Assess for malaria.
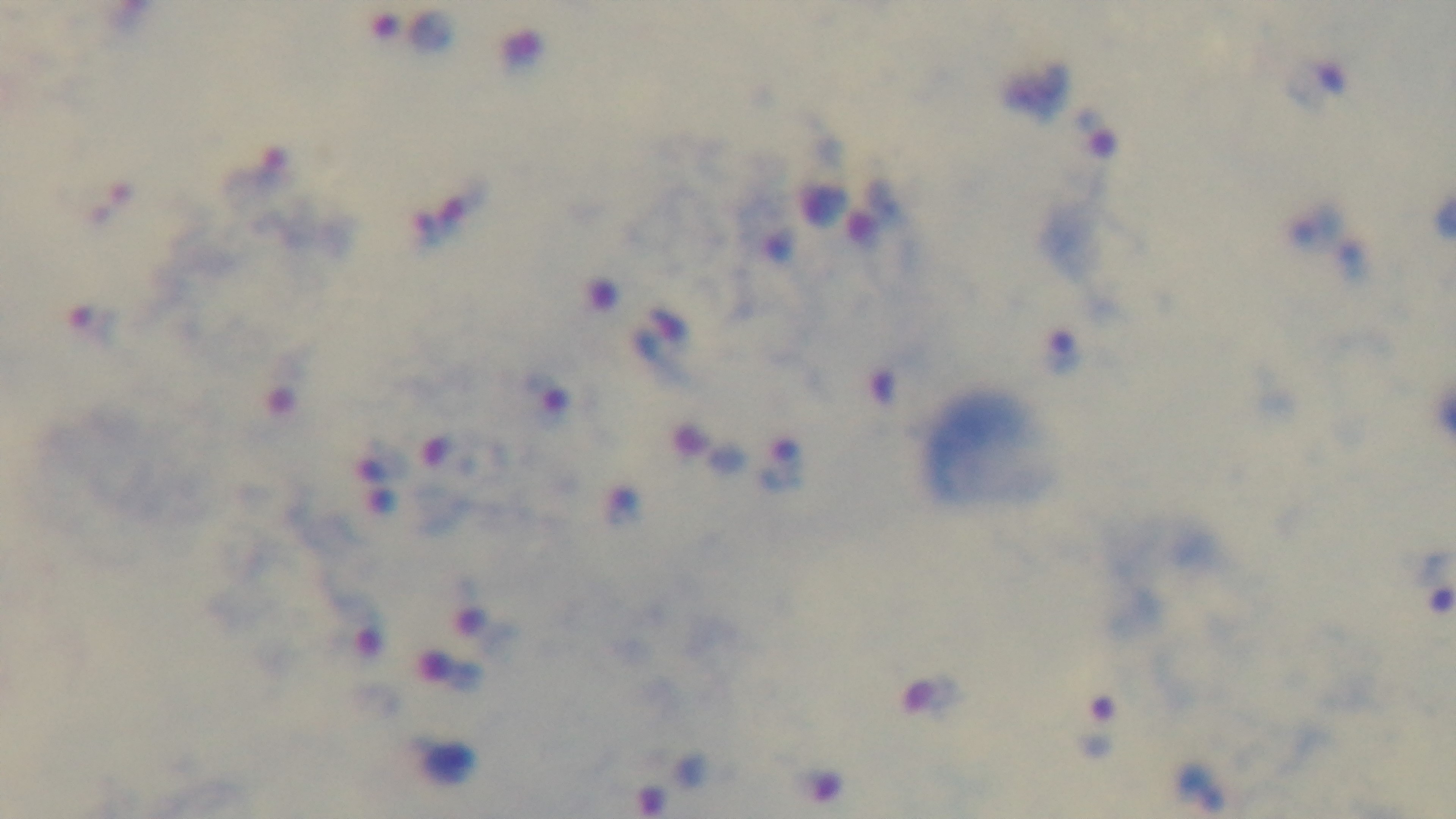

Infected.

Captured with a mounted 4K digital camera. Light microscopy. Giemsa stain. One field from the slide. Preparation: thick. Oil-immersion objective, 100x.